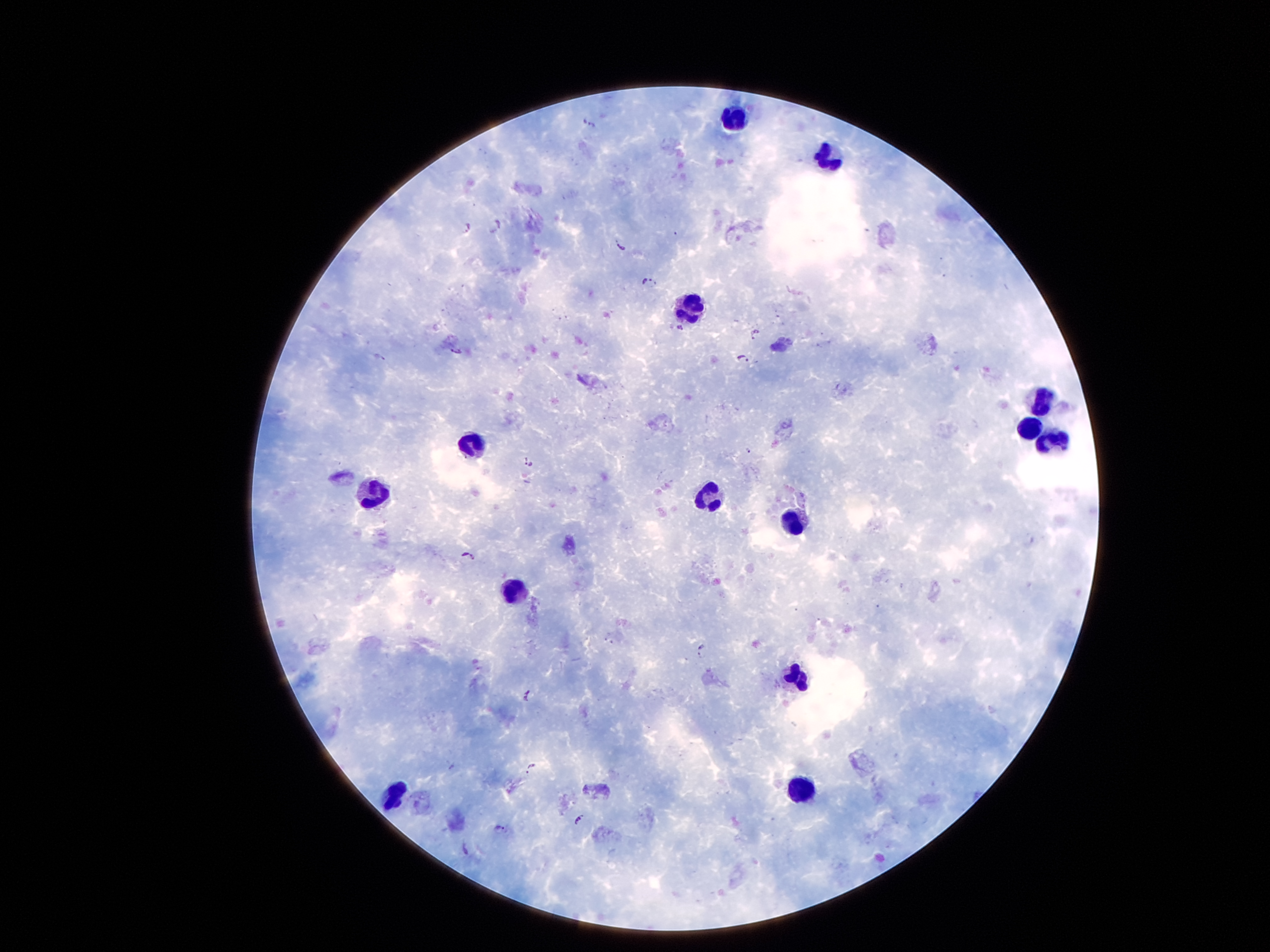
Approximate centers as [x, y] in pixels.
Summary:
  - Leukocyte locations: [735, 119], [826, 158], [689, 306], [1042, 403], [1029, 430], [470, 445], [1049, 446], [374, 494], [706, 497], [795, 520], [512, 594], [799, 678], [799, 787], [392, 793]
  - Plasmodium parasite locations: [589, 122], [498, 225], [465, 229], [621, 245], [650, 280], [681, 327], [755, 334], [379, 357], [742, 359], [750, 452], [527, 461], [467, 556], [701, 652], [528, 695], [530, 768], [578, 819], [500, 829], [467, 849]
  - Preparation: thick peripheral-blood smear
  - Stain: Giemsa
  - Capture: smartphone camera through the microscope eyepiece
  - Magnification: 100x
  - Image size: 1270×952 pixels
  - Field of view: one from this slide
  - Patient malaria status: positive for Plasmodium falciparum